Assess this cell for malaria.
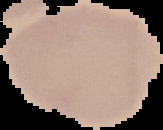
It is uninfected.

image_type: segmented cell region with the area outside set to black
image_size: 163×130 pixels
preparation: thin blood film